Report the malaria status of this cell.
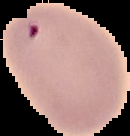

Parasitized.

Summary:
  - Image size: 130×136 pixels
  - Image type: segmented cell region with the area outside set to black
  - Preparation: thin blood film